Name the parasite shown.
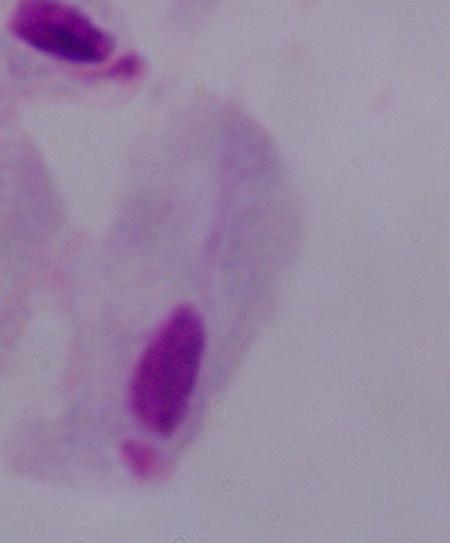
This is a trichomonad.

Photomicrograph. Captured at 1000x magnification.